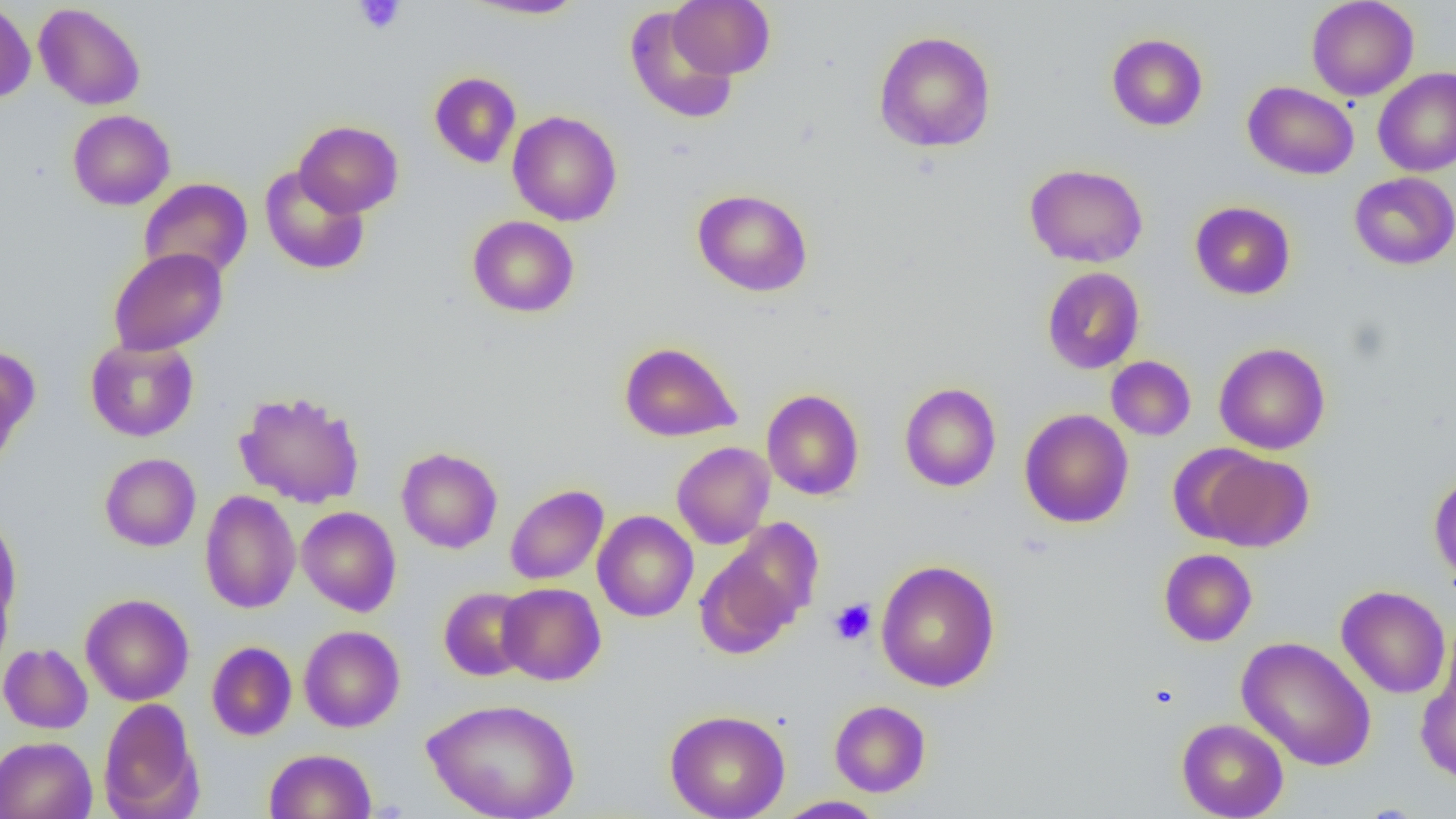

Approximate bounding boxes as (x1,y1)-(x2,y2) corner pairs in pixels. Uninfected red blood cell locations: (465,0)-(587,20), (668,0)-(774,80), (1306,0)-(1418,101), (0,1)-(36,104), (33,3)-(146,110), (624,5)-(739,124), (874,30)-(996,153), (1106,33)-(1208,131), (1373,67)-(1456,177), (429,72)-(521,168), (1243,81)-(1358,179), (67,109)-(175,210), (508,110)-(622,226), (294,120)-(404,218), (1024,163)-(1148,268), (259,166)-(370,275), (1349,172)-(1456,270), (138,178)-(253,282), (693,188)-(813,297), (1190,201)-(1296,300), (467,215)-(579,318), (108,247)-(228,356), (1042,267)-(1145,374), (85,337)-(199,442), (619,341)-(741,442), (1214,342)-(1330,455), (0,344)-(39,465), (1106,356)-(1196,441), (899,383)-(1001,492), (762,389)-(865,500), (234,390)-(366,508), (1019,409)-(1134,528), (672,441)-(775,549), (396,447)-(503,554), (1197,449)-(1315,552), (99,453)-(201,551), (1429,472)-(1456,586), (505,484)-(608,584), (199,490)-(301,614), (296,506)-(401,616), (592,510)-(699,622), (0,516)-(21,629), (721,518)-(825,629), (1158,548)-(1257,646), (695,551)-(800,658), (875,560)-(1000,692), (0,573)-(14,672), (497,582)-(606,685), (1336,585)-(1451,699), (439,586)-(534,681), (80,593)-(194,706), (299,625)-(405,732), (1237,636)-(1377,771), (206,640)-(297,741), (0,643)-(92,734), (1416,660)-(1456,784), (422,697)-(580,819), (98,698)-(202,818), (829,700)-(931,797), (665,709)-(790,819), (1177,717)-(1289,819), (0,736)-(97,819), (264,748)-(376,819), (776,796)-(886,818). Platelet locations: (354,0)-(405,34), (829,599)-(876,645). Slide-level diagnosis: negative for blood parasites. Thin blood film. Single field of view. Captured at 1000x magnification. Image is 1456×819 pixels. Optical microscopy.